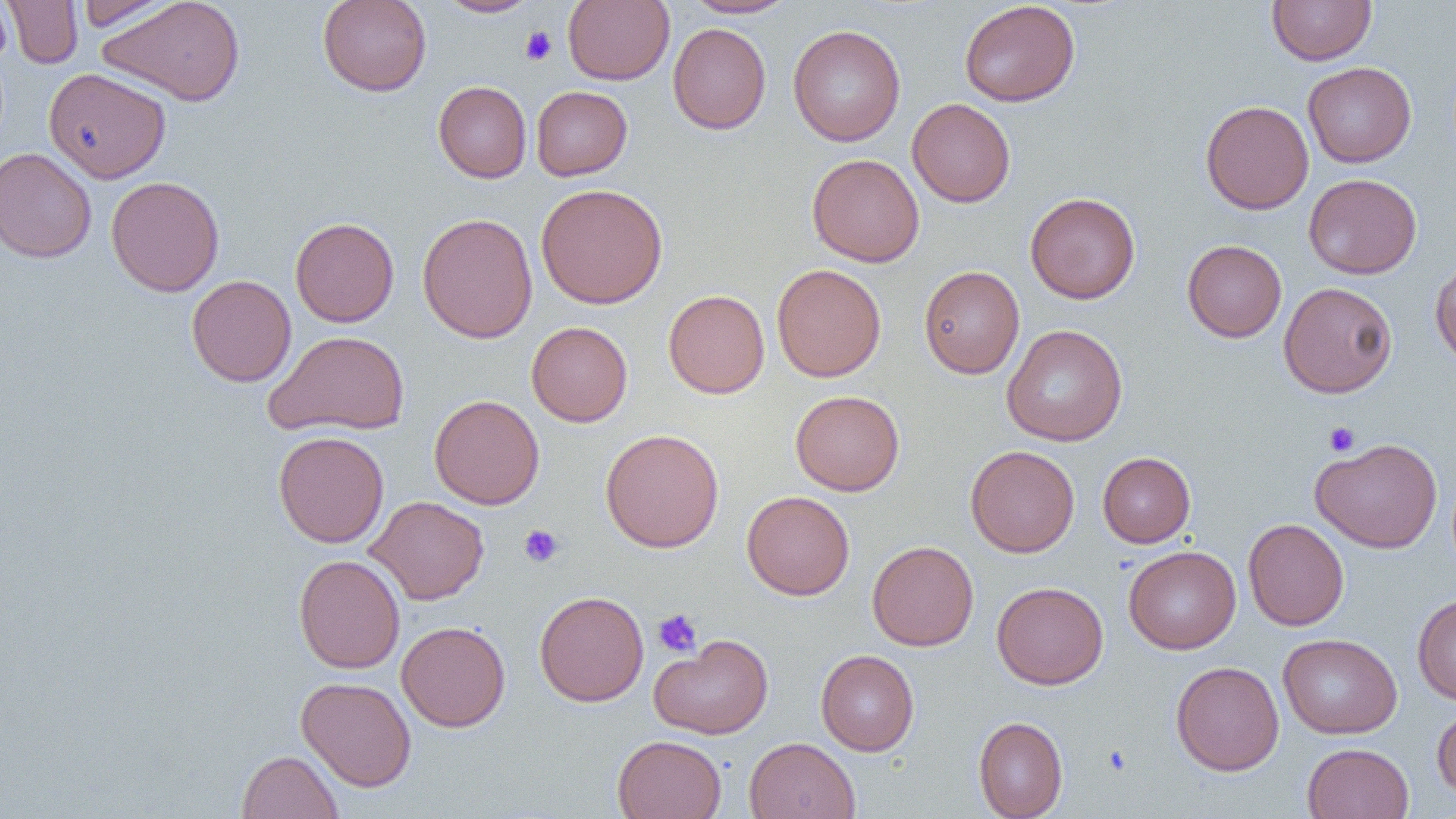

Approximate bounding boxes as named x1/y1/x2/y2 corners in pixels. Uninfected red blood cell locations: (x1=3, y1=0, x2=83, y2=69), (x1=75, y1=0, x2=178, y2=31), (x1=99, y1=0, x2=246, y2=106), (x1=317, y1=0, x2=432, y2=96), (x1=436, y1=0, x2=540, y2=18), (x1=562, y1=0, x2=674, y2=85), (x1=681, y1=0, x2=796, y2=18), (x1=1267, y1=0, x2=1377, y2=66), (x1=0, y1=1, x2=11, y2=64), (x1=959, y1=1, x2=1080, y2=107), (x1=668, y1=23, x2=771, y2=134), (x1=787, y1=24, x2=905, y2=146), (x1=1303, y1=61, x2=1417, y2=167), (x1=44, y1=67, x2=171, y2=183), (x1=433, y1=80, x2=532, y2=183), (x1=531, y1=85, x2=632, y2=180), (x1=907, y1=98, x2=1016, y2=207), (x1=1200, y1=100, x2=1314, y2=214), (x1=0, y1=147, x2=97, y2=263), (x1=807, y1=153, x2=924, y2=266), (x1=1303, y1=173, x2=1421, y2=279), (x1=106, y1=175, x2=225, y2=297), (x1=536, y1=183, x2=668, y2=309), (x1=1025, y1=192, x2=1140, y2=303), (x1=417, y1=212, x2=538, y2=343), (x1=290, y1=217, x2=399, y2=327), (x1=1182, y1=239, x2=1286, y2=342), (x1=1430, y1=257, x2=1456, y2=368), (x1=771, y1=263, x2=886, y2=382), (x1=918, y1=265, x2=1024, y2=378), (x1=186, y1=274, x2=296, y2=387), (x1=1279, y1=282, x2=1397, y2=397), (x1=663, y1=289, x2=769, y2=398), (x1=527, y1=321, x2=632, y2=426), (x1=1001, y1=324, x2=1128, y2=446), (x1=265, y1=330, x2=411, y2=437), (x1=790, y1=389, x2=905, y2=496), (x1=429, y1=394, x2=545, y2=509), (x1=600, y1=428, x2=725, y2=553), (x1=273, y1=431, x2=389, y2=548), (x1=1311, y1=437, x2=1442, y2=553), (x1=965, y1=444, x2=1079, y2=557), (x1=1098, y1=452, x2=1195, y2=547), (x1=741, y1=491, x2=855, y2=600), (x1=366, y1=495, x2=489, y2=605), (x1=1243, y1=518, x2=1349, y2=630), (x1=867, y1=540, x2=979, y2=651), (x1=1123, y1=545, x2=1241, y2=654), (x1=293, y1=554, x2=405, y2=673), (x1=991, y1=581, x2=1108, y2=689), (x1=534, y1=590, x2=649, y2=706), (x1=1412, y1=593, x2=1456, y2=704), (x1=396, y1=620, x2=510, y2=732), (x1=1278, y1=633, x2=1402, y2=738), (x1=649, y1=634, x2=773, y2=739), (x1=816, y1=650, x2=919, y2=755), (x1=1170, y1=660, x2=1284, y2=775), (x1=296, y1=676, x2=417, y2=791), (x1=1432, y1=705, x2=1456, y2=800), (x1=973, y1=716, x2=1068, y2=819), (x1=612, y1=734, x2=726, y2=819), (x1=744, y1=736, x2=860, y2=819), (x1=1302, y1=742, x2=1414, y2=819), (x1=237, y1=750, x2=343, y2=819). Platelet locations: (x1=520, y1=26, x2=558, y2=65), (x1=1323, y1=421, x2=1360, y2=456), (x1=519, y1=524, x2=564, y2=567), (x1=652, y1=609, x2=702, y2=657), (x1=1102, y1=745, x2=1131, y2=775). Slide-level diagnosis: negative for blood parasites. Thin blood film. Image is 1456×819 pixels. Optical microscopy. Captured at 1000x magnification. Single field of view.